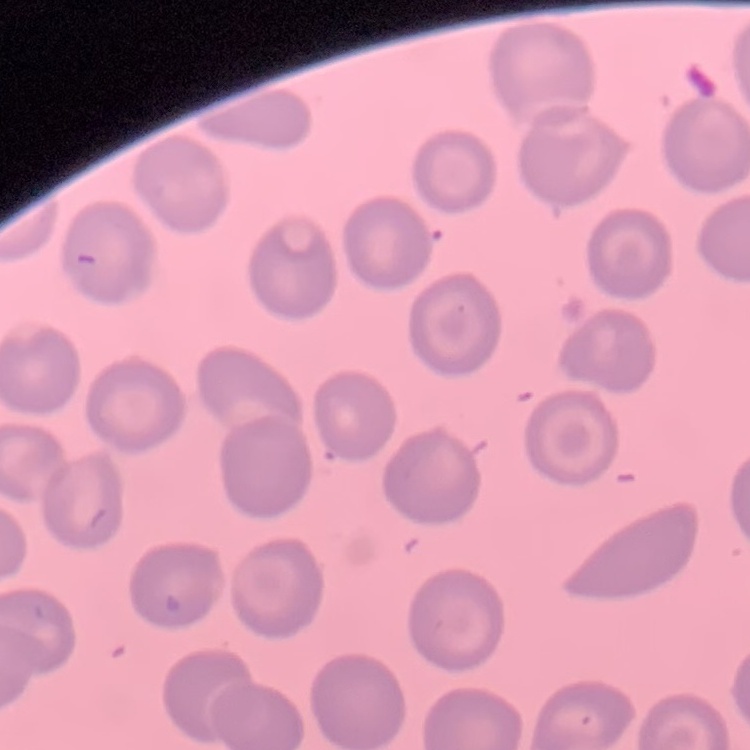

Summary:
  - Red blood cell morphology: no rouleaux formation
  - Preparation: thin blood smear
  - Image type: one tile cut from a larger photomicrograph
  - Stain: Field's or Giemsa